Classify this cell by malaria status.
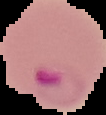
It is parasitized.

image type = segmented cell region with the area outside set to black
image size = 106×115 pixels
preparation = thin blood film